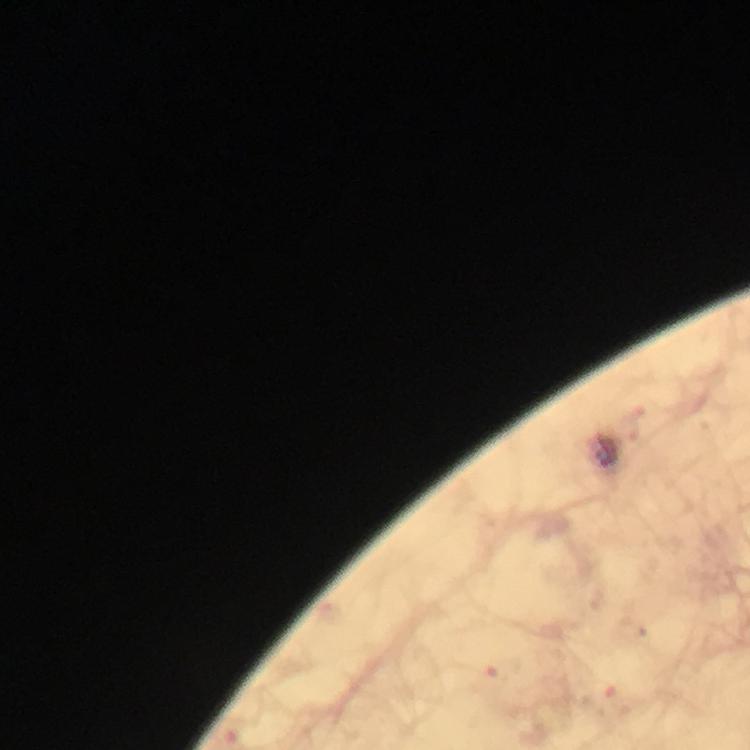 Approximate object centers, in pixels from the top-left corner. Malaria parasite locations: (x=505, y=671), (x=614, y=704). Thick blood smear. Immersion oil applied. Photographed through the microscope with a smartphone camera. From a malaria diagnostic workup. Image is 750×750 pixels. At 100x magnification. A crop from one field of view. Giemsa stain.